Locate every uninfected red blood cell.
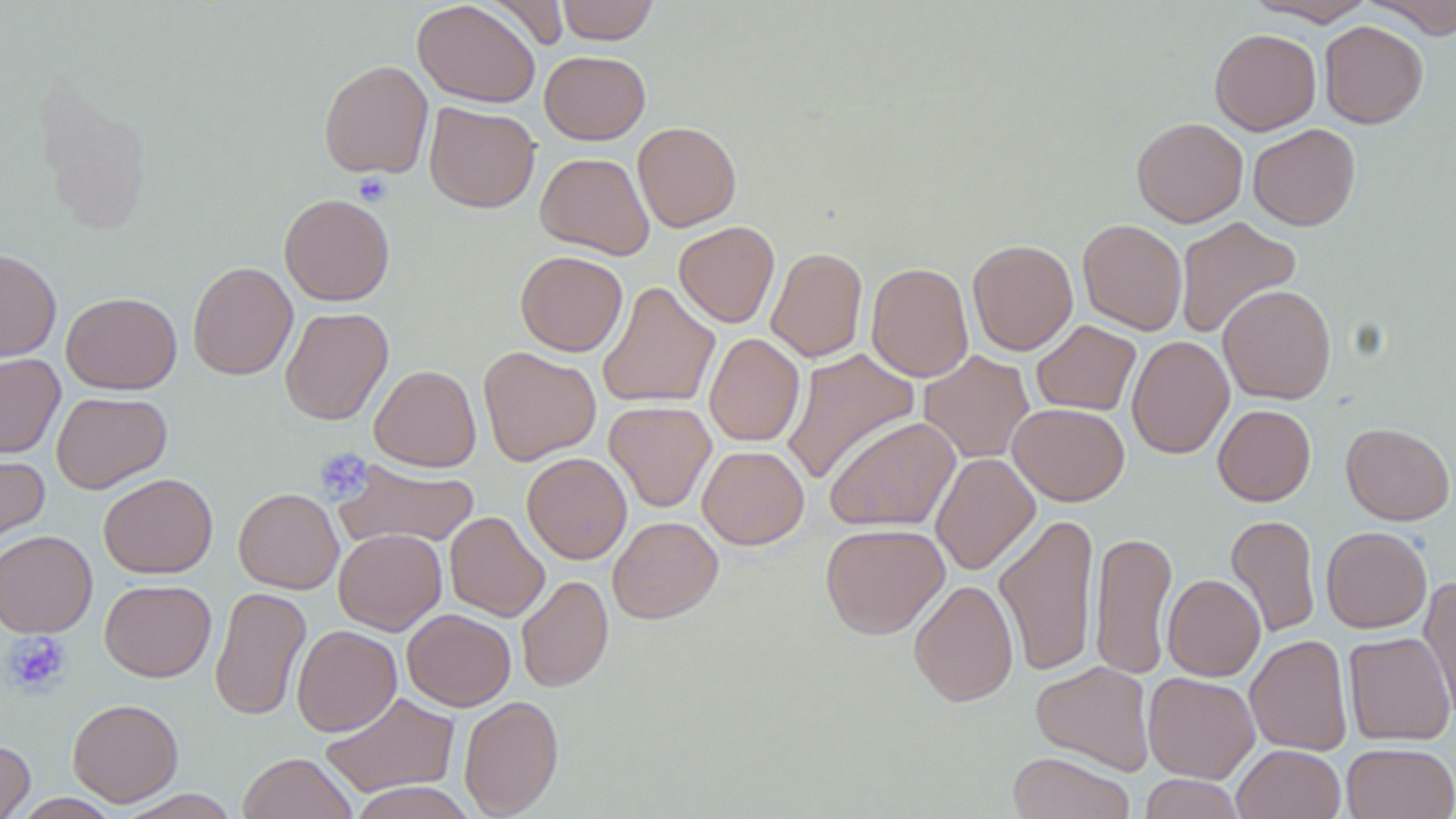
Approximate bounding boxes as (x1,y1)-(x2,y2) corner pairs in pixels.
Uninfected red blood cells: (487,0)-(569,51), (556,0)-(658,44), (1245,0)-(1376,26), (1361,0)-(1456,38), (412,1)-(541,108), (1319,20)-(1429,128), (1209,28)-(1321,135), (539,51)-(650,144), (318,60)-(433,179), (424,102)-(540,213), (1131,117)-(1248,227), (633,121)-(741,232), (1248,123)-(1361,231), (535,152)-(654,259), (279,193)-(395,305), (1174,216)-(1301,340), (1077,218)-(1187,335), (674,221)-(779,328), (967,239)-(1078,355), (766,247)-(868,363), (0,248)-(61,362), (516,251)-(627,356), (187,261)-(298,381), (866,261)-(973,382), (596,281)-(720,409), (1218,284)-(1337,404), (61,291)-(182,394), (280,307)-(394,425), (1031,320)-(1141,416), (704,333)-(805,447), (1126,335)-(1234,460), (478,346)-(601,466), (781,348)-(921,485), (919,350)-(1034,463), (0,353)-(65,458), (370,365)-(481,471), (51,391)-(172,493), (604,400)-(716,512), (1008,402)-(1129,506), (1213,404)-(1316,506), (823,416)-(961,533), (1341,422)-(1454,525), (697,445)-(809,549), (0,451)-(50,553), (522,452)-(632,564), (930,452)-(1040,576), (335,460)-(480,550), (98,473)-(217,579), (234,488)-(343,594), (445,511)-(549,622), (993,512)-(1099,677), (1225,514)-(1321,638), (608,516)-(723,624), (820,523)-(950,639), (1321,526)-(1432,633), (334,528)-(446,635), (0,530)-(97,637), (1089,530)-(1176,680), (516,574)-(613,693), (1163,574)-(1265,681), (1419,575)-(1456,722), (908,578)-(1019,708), (100,579)-(217,682), (209,586)-(311,722), (402,608)-(516,711), (292,625)-(402,736), (1343,631)-(1455,746), (1246,634)-(1353,756), (1030,661)-(1155,775), (1143,672)-(1260,783), (320,692)-(460,797), (459,694)-(564,818), (67,698)-(183,806), (0,740)-(35,819), (1342,742)-(1456,819), (1233,744)-(1345,819), (1008,751)-(1134,819), (238,752)-(357,818), (1140,774)-(1245,819), (348,782)-(478,818), (118,789)-(241,818), (10,793)-(123,818).

Summary:
  - Platelet locations: (353,173)-(392,205), (314,447)-(373,503), (1,631)-(72,696)
  - Slide-level diagnosis: negative for blood parasites
  - Magnification: 1000x
  - Field of view: one of a larger specimen
  - Modality: light microscopy
  - Preparation: thin blood smear
  - Image size: 1456×819 pixels
  - Stain: May-Grünwald-Giemsa